Locate every blood parasite and identify its species.
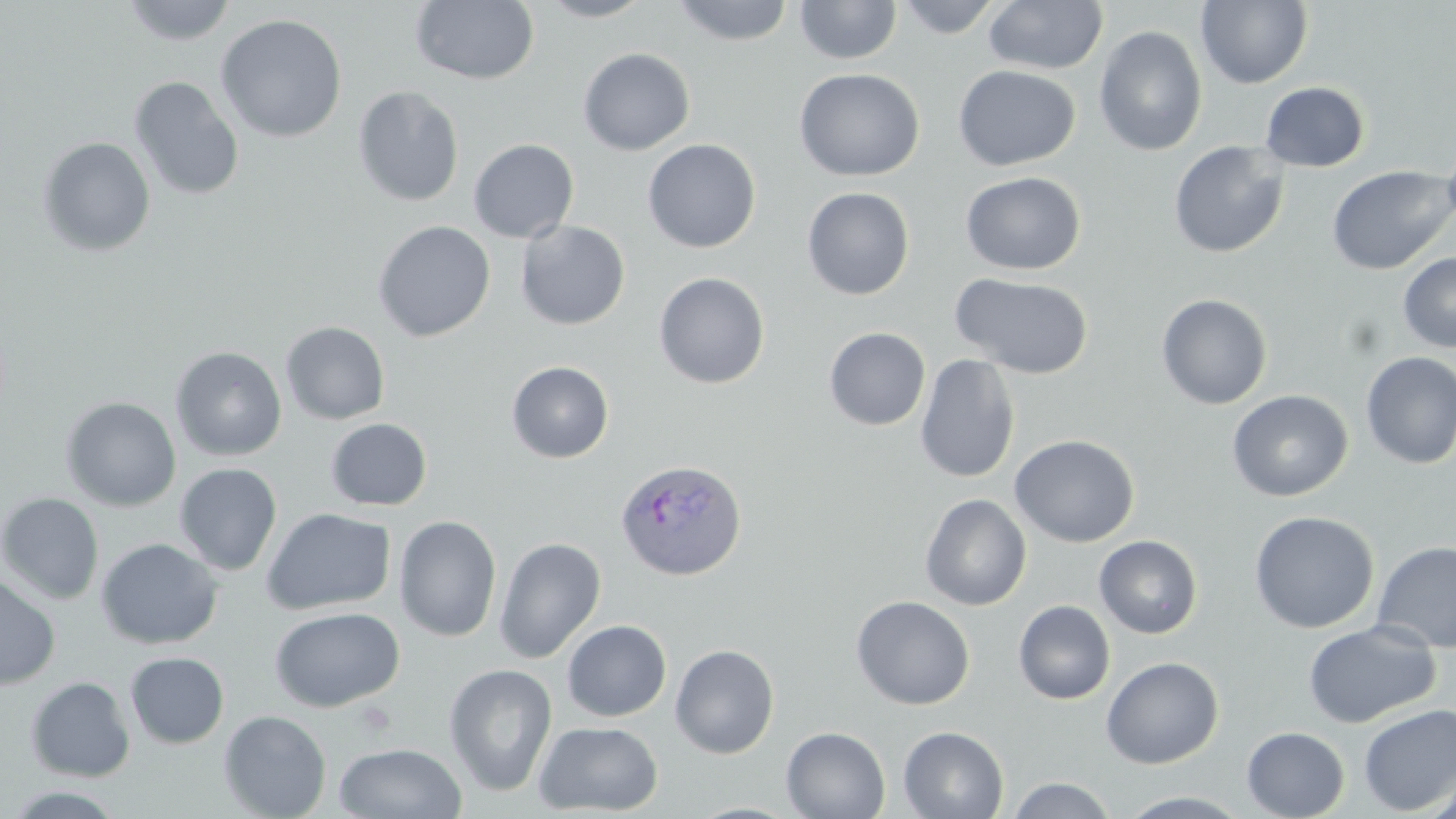
Approximate bounding boxes as named x1/y1/x2/y2 corners in pixels.
Plasmodium ovale-infected red blood cells: (x1=615, y1=457, x2=748, y2=580).
No Plasmodium falciparum, Plasmodium malariae, Plasmodium vivax, Babesia divergens, or Trypanosoma brucei observed.

slide-level diagnosis = Plasmodium ovale
stain = May-Grünwald-Giemsa
uninfected red blood cell locations = approximate bounding boxes as named x1/y1/x2/y2 corners in pixels: (x1=121, y1=0, x2=237, y2=46), (x1=410, y1=0, x2=540, y2=85), (x1=538, y1=0, x2=655, y2=22), (x1=670, y1=0, x2=796, y2=46), (x1=893, y1=0, x2=1004, y2=38), (x1=983, y1=0, x2=1107, y2=74), (x1=1196, y1=0, x2=1313, y2=89), (x1=795, y1=1, x2=903, y2=65), (x1=215, y1=14, x2=347, y2=143), (x1=1094, y1=25, x2=1208, y2=156), (x1=577, y1=47, x2=695, y2=156), (x1=953, y1=64, x2=1081, y2=170), (x1=793, y1=68, x2=924, y2=181), (x1=129, y1=76, x2=244, y2=201), (x1=1260, y1=81, x2=1371, y2=173), (x1=352, y1=86, x2=465, y2=207), (x1=1442, y1=135, x2=1456, y2=233), (x1=37, y1=136, x2=156, y2=257), (x1=468, y1=138, x2=579, y2=243), (x1=642, y1=138, x2=761, y2=253), (x1=1168, y1=140, x2=1290, y2=258), (x1=1326, y1=165, x2=1455, y2=275), (x1=960, y1=172, x2=1085, y2=275), (x1=801, y1=187, x2=915, y2=300), (x1=372, y1=220, x2=496, y2=342), (x1=515, y1=220, x2=630, y2=330), (x1=1398, y1=252, x2=1456, y2=352), (x1=653, y1=272, x2=771, y2=389), (x1=950, y1=272, x2=1094, y2=379), (x1=1155, y1=293, x2=1273, y2=410), (x1=280, y1=321, x2=391, y2=425), (x1=824, y1=327, x2=931, y2=430), (x1=170, y1=346, x2=287, y2=461), (x1=1360, y1=352, x2=1456, y2=470), (x1=914, y1=354, x2=1021, y2=484), (x1=505, y1=360, x2=614, y2=463), (x1=1227, y1=389, x2=1354, y2=501), (x1=61, y1=396, x2=181, y2=511), (x1=326, y1=418, x2=433, y2=511), (x1=1009, y1=434, x2=1140, y2=547), (x1=174, y1=463, x2=282, y2=576), (x1=0, y1=492, x2=104, y2=605), (x1=920, y1=494, x2=1032, y2=610), (x1=260, y1=507, x2=396, y2=615), (x1=1249, y1=510, x2=1379, y2=634), (x1=394, y1=515, x2=502, y2=642), (x1=1094, y1=535, x2=1203, y2=638), (x1=494, y1=537, x2=607, y2=663), (x1=96, y1=538, x2=223, y2=649), (x1=1372, y1=541, x2=1456, y2=654), (x1=0, y1=574, x2=60, y2=690), (x1=851, y1=595, x2=975, y2=710), (x1=1013, y1=600, x2=1115, y2=705), (x1=270, y1=606, x2=405, y2=712), (x1=562, y1=619, x2=671, y2=721), (x1=1302, y1=620, x2=1441, y2=728), (x1=670, y1=643, x2=780, y2=759), (x1=124, y1=651, x2=229, y2=749), (x1=1101, y1=657, x2=1224, y2=769), (x1=444, y1=663, x2=557, y2=796), (x1=25, y1=676, x2=135, y2=782), (x1=1358, y1=704, x2=1456, y2=815), (x1=219, y1=710, x2=332, y2=819), (x1=533, y1=721, x2=664, y2=816), (x1=781, y1=726, x2=890, y2=818), (x1=897, y1=726, x2=1009, y2=819), (x1=1241, y1=726, x2=1350, y2=819), (x1=333, y1=742, x2=468, y2=818), (x1=1422, y1=772, x2=1456, y2=819), (x1=1005, y1=775, x2=1118, y2=818), (x1=4, y1=786, x2=130, y2=818), (x1=1116, y1=790, x2=1253, y2=818), (x1=684, y1=801, x2=804, y2=819)
modality = optical microscopy
magnification = 1000x
field of view = one of a larger specimen
image size = 1456×819 pixels
preparation = thin blood film